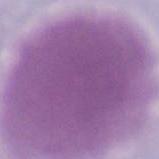

identification = erythrocyte
modality = photomicrograph
magnification = 1000x